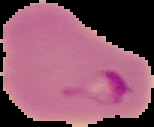
Summary:
  - Image size: 154×127 pixels
  - Image type: segmented cell region with the area outside set to black
  - Result: malaria parasites detected
  - Preparation: thin blood smear